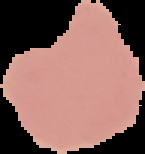

preparation: thin blood smear
result: no malaria parasites seen
image_type: cell region segmented out of the field of view; surrounding area masked to black
image_size: 145×154 pixels